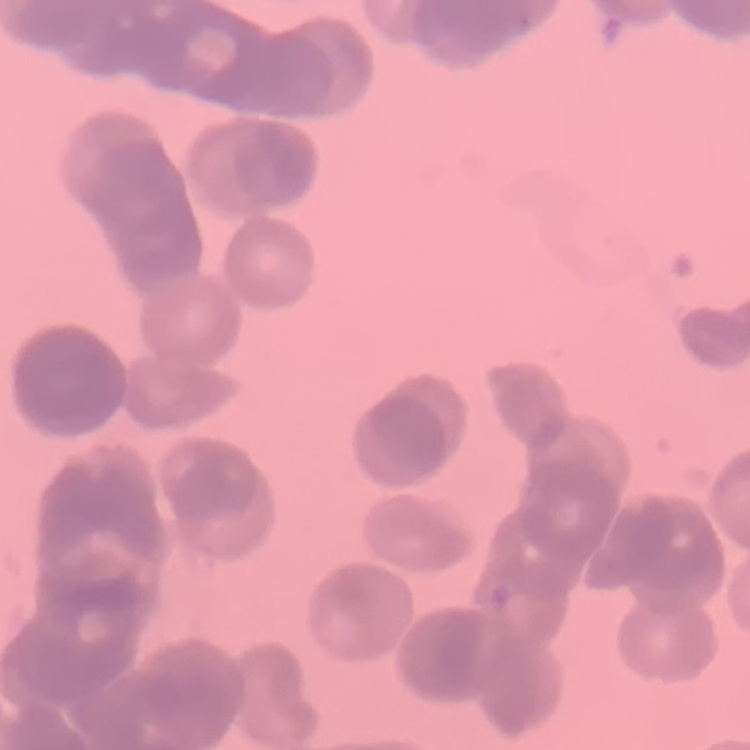
The erythrocytes show rouleaux formation. One tile cut from a larger photomicrograph. Thin peripheral smear. Field's or Giemsa stain.